Assess the morphology of the erythrocytes.
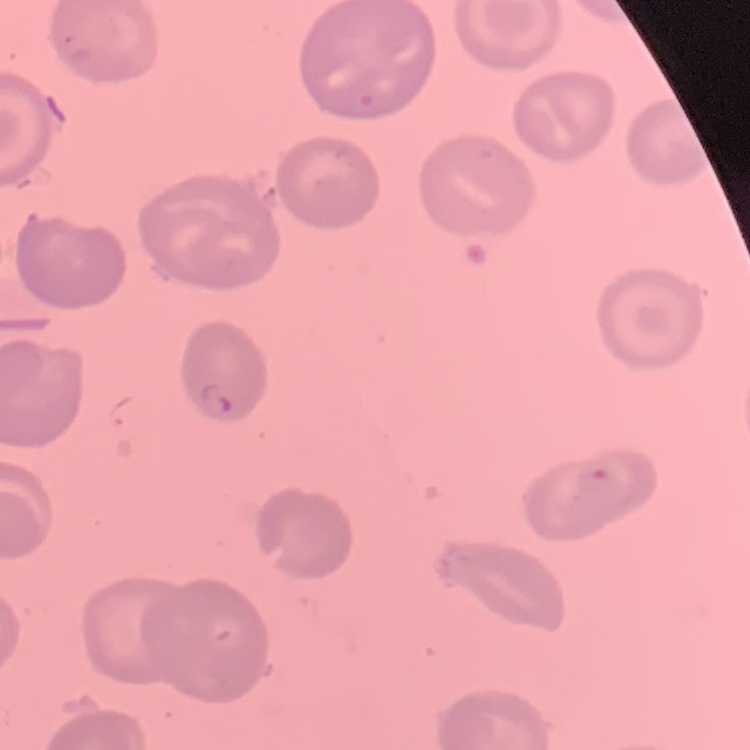
No rouleaux formation.

{
  "image_type": "square crop of a larger photomicrograph",
  "preparation": "thin blood film",
  "stain": "Field's or Giemsa"
}